State which parasite is depicted.
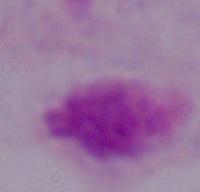

This is a trichomonad.

1000x magnification. Micrograph.